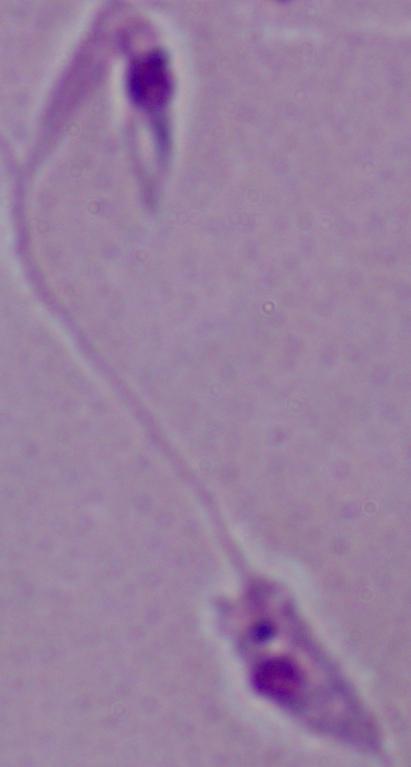 A Leishmania parasite is seen. Micrograph. Captured at 1000x magnification.